Report the malaria status of this cell.
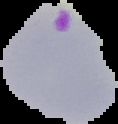
Parasitized.

From a thin blood film. Image is 118×124 pixels. Cell region segmented out of the field of view; the surrounding area is masked to black.